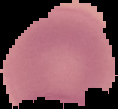
Summary:
  - Image size: 118×109 pixels
  - Image type: segmented cell region with the area outside set to black
  - Preparation: thin blood smear
  - Result: negative for malaria parasites